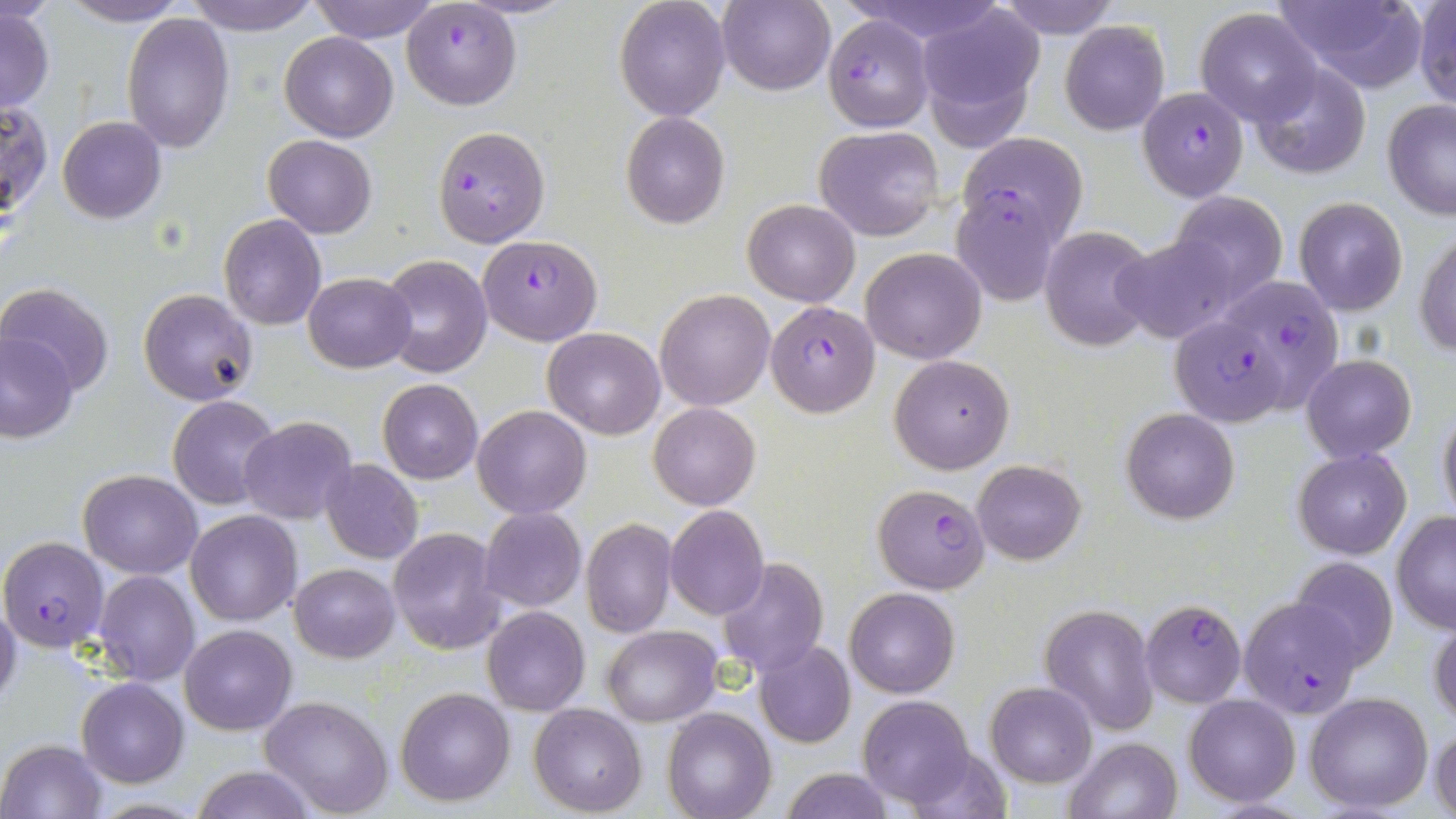

Summary:
  - Coordinate format: approximate bounding boxes as (x1, y1, x2, y2) in pixels
  - Uninfected red blood cell locations: (61, 0, 187, 26), (183, 0, 320, 34), (308, 0, 441, 42), (615, 0, 731, 121), (990, 0, 1123, 40), (1277, 0, 1431, 92), (1413, 0, 1456, 111), (717, 1, 836, 96), (916, 5, 1045, 146), (1, 6, 54, 113), (1195, 7, 1323, 126), (120, 12, 235, 153), (1060, 21, 1169, 135), (280, 32, 398, 142), (1249, 64, 1371, 180), (1381, 99, 1455, 220), (0, 102, 50, 220), (621, 112, 730, 229), (58, 116, 166, 222), (814, 126, 945, 242), (960, 133, 1087, 243), (264, 134, 377, 237), (1168, 190, 1288, 306), (1292, 196, 1409, 316), (743, 199, 860, 306), (218, 214, 327, 330), (1039, 225, 1158, 352), (1416, 228, 1456, 357), (1113, 233, 1243, 345), (861, 247, 985, 364), (379, 254, 493, 377), (303, 272, 417, 373), (1, 283, 114, 393), (140, 290, 257, 405), (655, 290, 776, 410), (543, 328, 666, 439), (1, 332, 78, 443), (889, 354, 1014, 475), (1302, 355, 1415, 462), (378, 379, 483, 484), (168, 394, 283, 509), (1437, 401, 1456, 526), (649, 402, 760, 509), (472, 404, 592, 519), (1120, 408, 1239, 524), (239, 416, 357, 524), (1292, 447, 1411, 559), (973, 459, 1086, 564), (320, 460, 424, 564), (78, 468, 202, 578), (62, 476, 195, 668), (665, 505, 768, 620), (480, 507, 586, 612), (186, 511, 303, 626), (1390, 511, 1456, 632), (582, 518, 676, 637), (387, 527, 504, 655), (718, 556, 827, 679), (1288, 557, 1400, 671), (288, 563, 399, 662), (93, 569, 201, 686), (846, 587, 960, 698), (0, 595, 22, 710), (1039, 604, 1158, 735), (482, 605, 589, 716), (1428, 612, 1456, 729), (179, 623, 297, 734), (602, 625, 721, 728), (754, 640, 856, 749), (77, 678, 188, 787), (986, 682, 1095, 787), (395, 686, 516, 806), (1304, 691, 1433, 813), (1185, 694, 1299, 807), (258, 695, 395, 817), (857, 695, 975, 810), (530, 704, 646, 815), (663, 708, 776, 819), (1429, 727, 1456, 818), (1065, 736, 1182, 819), (1, 737, 106, 818), (904, 742, 1009, 818), (191, 766, 319, 819), (782, 767, 893, 819)
  - Plasmodium falciparum-infected red blood cell locations: (401, 1, 521, 110), (823, 16, 934, 131), (1138, 86, 1249, 202), (432, 126, 550, 247), (953, 189, 1064, 307), (480, 233, 601, 345), (1229, 277, 1349, 410), (766, 301, 879, 417), (1170, 315, 1286, 426), (872, 483, 991, 594), (0, 536, 108, 650), (1237, 598, 1363, 718), (1139, 601, 1247, 707)
  - Slide-level diagnosis: Plasmodium falciparum
  - Preparation: thin blood smear
  - Image size: 1456×819 pixels
  - Modality: optical microscopy
  - Field of view: one of a larger specimen
  - Magnification: 1000x
  - Stain: May-Grünwald-Giemsa